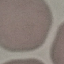
Summary:
  - Malaria status: uninfected
  - Image type: automatically extracted cell patch, resized to 64 × 64 pixels
  - Stain: Giemsa
  - Capture: smartphone camera at the microscope eyepiece
  - Preparation: thin smear